Locate every blood parasite and identify its species.
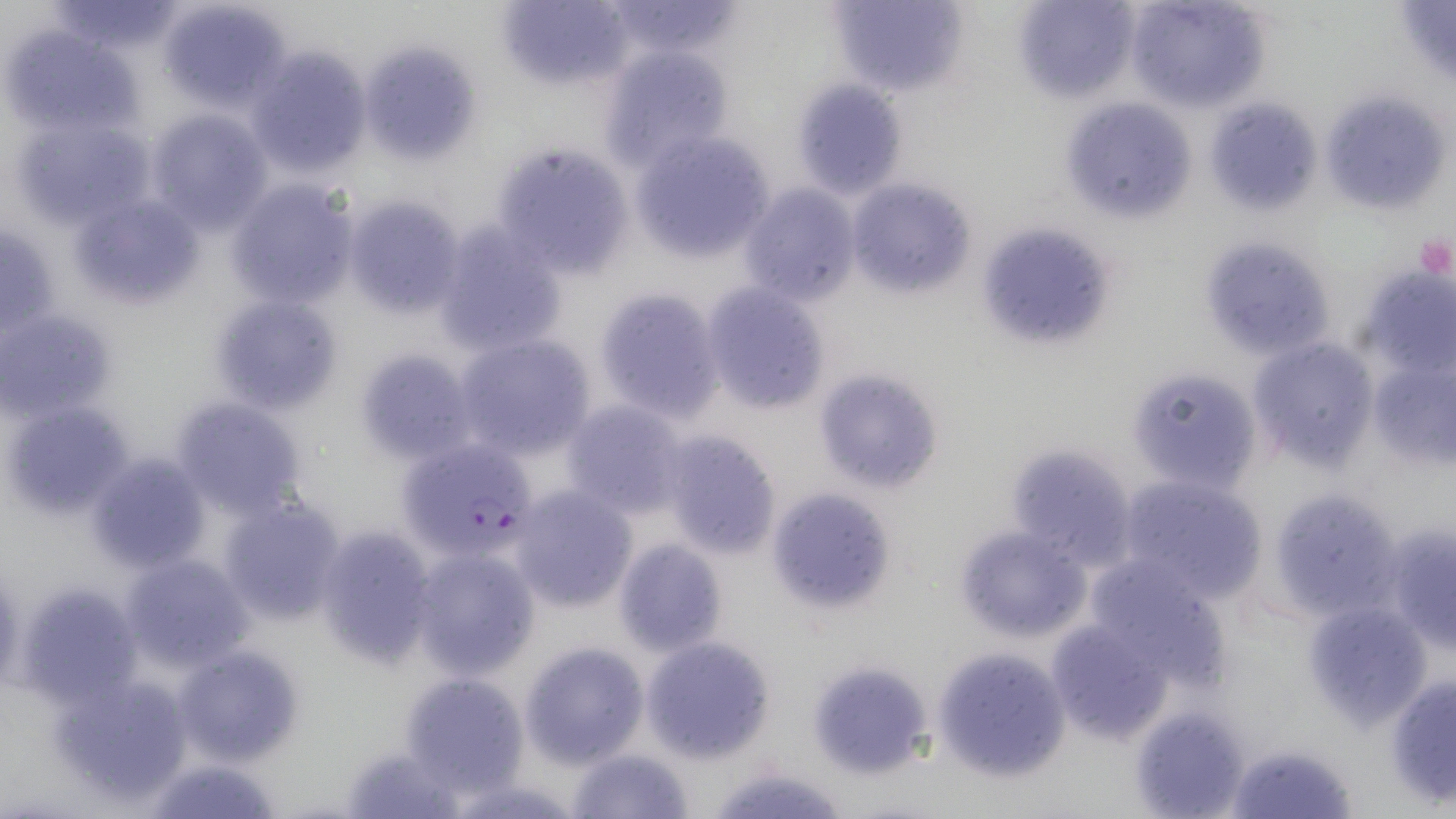
Approximate bounding boxes as named x1/y1/x2/y2 corners in pixels.
Plasmodium falciparum-infected red blood cells: (x1=396, y1=438, x2=540, y2=565).
No Plasmodium ovale, Plasmodium malariae, Plasmodium vivax, Babesia divergens, or Trypanosoma brucei observed.

Summary:
  - Uninfected red blood cell locations: (x1=158, y1=0, x2=292, y2=111), (x1=497, y1=0, x2=631, y2=90), (x1=603, y1=0, x2=745, y2=60), (x1=825, y1=0, x2=970, y2=99), (x1=1013, y1=0, x2=1140, y2=104), (x1=1124, y1=0, x2=1270, y2=111), (x1=50, y1=1, x2=183, y2=56), (x1=5, y1=28, x2=130, y2=133), (x1=359, y1=39, x2=481, y2=166), (x1=599, y1=45, x2=735, y2=171), (x1=247, y1=46, x2=373, y2=180), (x1=792, y1=79, x2=907, y2=199), (x1=1062, y1=97, x2=1197, y2=224), (x1=1323, y1=98, x2=1440, y2=214), (x1=1217, y1=107, x2=1322, y2=212), (x1=145, y1=108, x2=272, y2=231), (x1=16, y1=116, x2=148, y2=222), (x1=632, y1=133, x2=775, y2=262), (x1=491, y1=143, x2=631, y2=274), (x1=847, y1=179, x2=976, y2=297), (x1=226, y1=180, x2=359, y2=307), (x1=737, y1=184, x2=861, y2=306), (x1=342, y1=195, x2=468, y2=319), (x1=72, y1=204, x2=208, y2=308), (x1=432, y1=223, x2=564, y2=355), (x1=987, y1=229, x2=1111, y2=355), (x1=1198, y1=234, x2=1336, y2=363), (x1=1359, y1=263, x2=1452, y2=375), (x1=700, y1=282, x2=831, y2=413), (x1=595, y1=288, x2=726, y2=419), (x1=212, y1=295, x2=341, y2=416), (x1=4, y1=312, x2=114, y2=425), (x1=453, y1=334, x2=596, y2=460), (x1=1249, y1=337, x2=1379, y2=471), (x1=356, y1=349, x2=476, y2=461), (x1=1367, y1=352, x2=1456, y2=473), (x1=1125, y1=367, x2=1260, y2=496), (x1=813, y1=368, x2=945, y2=494), (x1=170, y1=396, x2=307, y2=516), (x1=560, y1=399, x2=689, y2=517), (x1=5, y1=402, x2=130, y2=515), (x1=656, y1=429, x2=784, y2=559), (x1=1004, y1=443, x2=1138, y2=567), (x1=89, y1=454, x2=210, y2=571), (x1=1115, y1=475, x2=1266, y2=603), (x1=509, y1=485, x2=637, y2=613), (x1=766, y1=487, x2=896, y2=615), (x1=1269, y1=488, x2=1404, y2=618), (x1=218, y1=497, x2=349, y2=626), (x1=1380, y1=520, x2=1456, y2=647), (x1=315, y1=525, x2=440, y2=666), (x1=954, y1=525, x2=1092, y2=642), (x1=614, y1=538, x2=728, y2=654), (x1=407, y1=545, x2=541, y2=679), (x1=119, y1=552, x2=253, y2=671), (x1=1082, y1=555, x2=1227, y2=683), (x1=20, y1=583, x2=142, y2=702), (x1=1306, y1=599, x2=1432, y2=727), (x1=1045, y1=620, x2=1170, y2=746), (x1=643, y1=636, x2=775, y2=761), (x1=521, y1=641, x2=649, y2=767), (x1=172, y1=644, x2=304, y2=766), (x1=933, y1=645, x2=1069, y2=778), (x1=815, y1=663, x2=934, y2=778), (x1=50, y1=669, x2=194, y2=806), (x1=400, y1=672, x2=529, y2=796), (x1=1387, y1=674, x2=1456, y2=804), (x1=1131, y1=705, x2=1252, y2=818), (x1=1227, y1=741, x2=1359, y2=819), (x1=338, y1=742, x2=463, y2=817), (x1=569, y1=748, x2=694, y2=819), (x1=141, y1=756, x2=282, y2=818), (x1=709, y1=764, x2=851, y2=819)
  - Platelet locations: (x1=1412, y1=234, x2=1455, y2=281)
  - Slide-level diagnosis: Plasmodium falciparum
  - Image size: 1456×819 pixels
  - Magnification: 1000x
  - Field of view: single
  - Preparation: thin blood film
  - Modality: light microscopy
  - Stain: May-Grünwald-Giemsa